Classify this cell by malaria status.
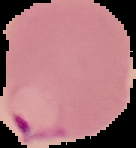
It is parasitized.

{
  "image_size": "136×148 pixels",
  "image_type": "cell region segmented out of the field of view; surrounding area masked to black",
  "preparation": "thin blood smear"
}